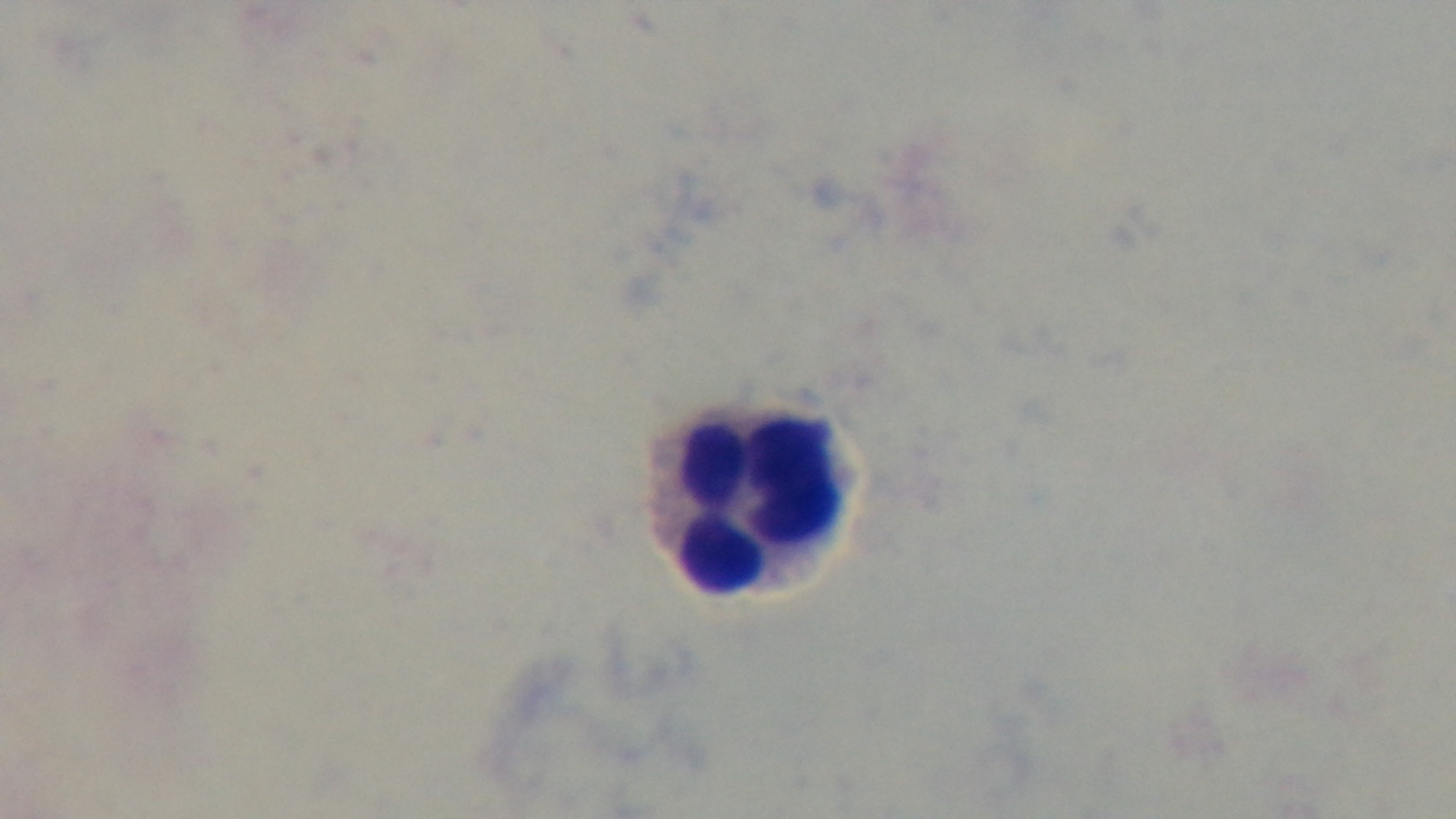

preparation: thick smear
stain: Giemsa
capture: mounted 4K digital camera
malaria_status: uninfected
field_of_view: single
objective: 100x oil immersion
modality: light microscopy